Outline each blood parasite and name the species.
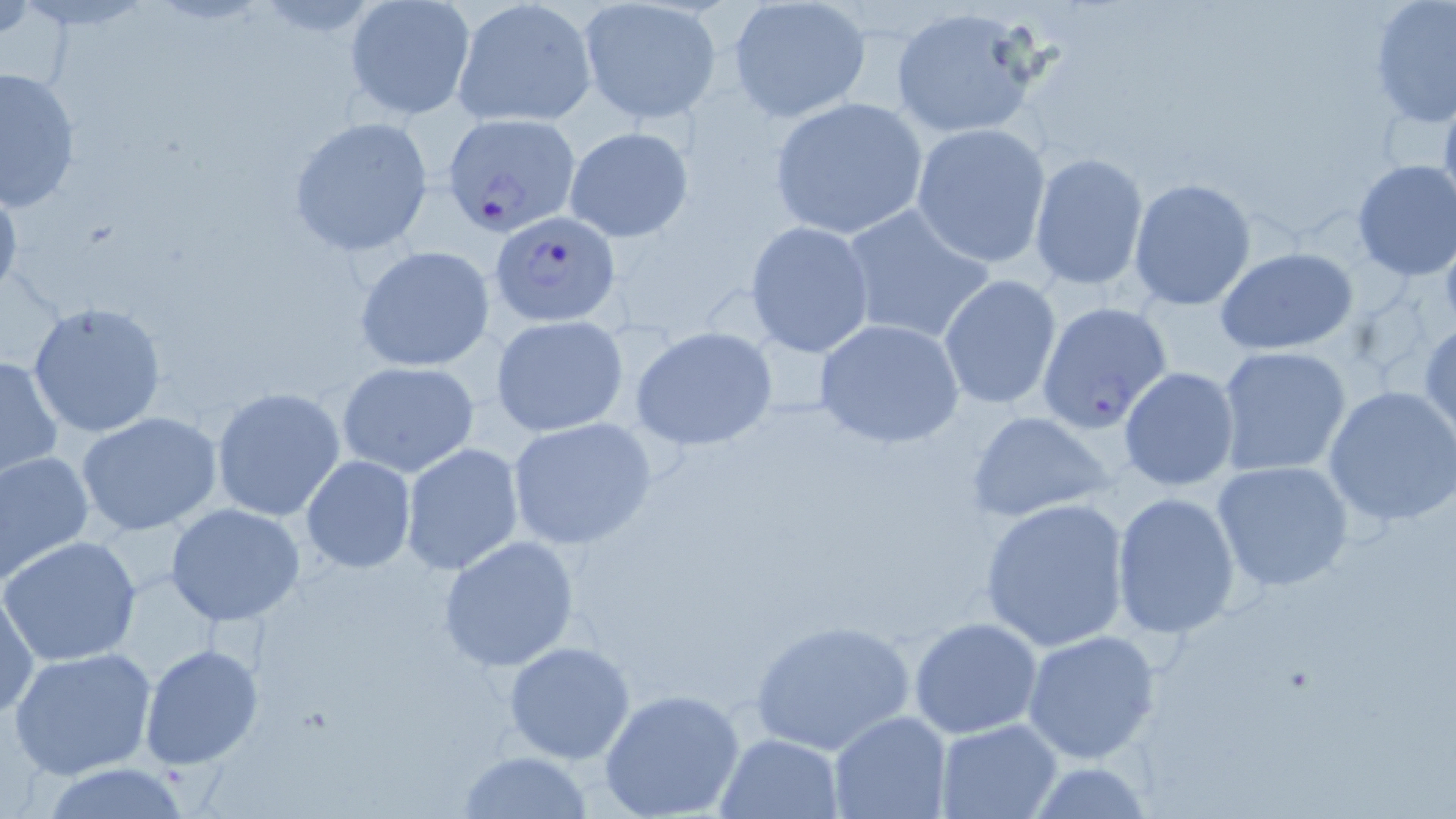

Approximate bounding boxes as [x1, y1, x2, y2] in pixels.
Plasmodium falciparum-infected red blood cells: [441, 112, 581, 238], [490, 212, 622, 327].
No Plasmodium ovale, Plasmodium malariae, Plasmodium vivax, Babesia divergens, or Trypanosoma brucei observed.

Uninfected red blood cell locations: [576, 0, 724, 124], [342, 1, 475, 121], [727, 1, 873, 124], [1368, 1, 1455, 129], [449, 2, 595, 128], [885, 6, 1050, 141], [2, 66, 81, 213], [1437, 89, 1456, 223], [768, 97, 928, 239], [288, 115, 436, 257], [910, 123, 1052, 267], [564, 126, 694, 242], [1027, 152, 1149, 292], [1350, 159, 1456, 281], [1128, 177, 1257, 309], [0, 181, 23, 303], [840, 202, 995, 347], [744, 218, 875, 357], [354, 245, 497, 373], [1215, 246, 1360, 356], [939, 273, 1063, 411], [25, 299, 170, 438], [1036, 300, 1175, 432], [492, 315, 628, 436], [811, 318, 966, 450], [1419, 321, 1456, 445], [630, 325, 777, 452], [1217, 346, 1354, 478], [0, 355, 64, 482], [337, 361, 481, 478], [1118, 367, 1241, 492], [1324, 384, 1456, 527], [211, 386, 346, 522], [965, 409, 1120, 525], [77, 411, 226, 537], [506, 416, 658, 550], [401, 443, 524, 576], [0, 449, 94, 585], [299, 456, 416, 572], [1211, 459, 1355, 592], [1110, 491, 1242, 638], [979, 496, 1131, 652], [166, 503, 307, 627], [437, 535, 583, 672], [2, 537, 142, 667], [1, 588, 40, 718], [909, 616, 1042, 739], [746, 618, 917, 756], [1022, 629, 1164, 764], [503, 640, 635, 763], [140, 643, 265, 769], [8, 647, 158, 779], [598, 687, 746, 819], [827, 711, 949, 819], [935, 719, 1063, 818], [716, 732, 844, 817], [458, 750, 594, 819], [1017, 760, 1160, 817], [35, 762, 198, 817]. Slide-level diagnosis: Plasmodium falciparum. Light microscopy. Thin blood film. 1000x magnification. Image is 1456×819 pixels. One field of a larger specimen. May-Grünwald-Giemsa stain.